Report the malaria status of this cell.
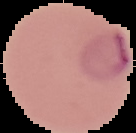
It is parasitized.

The area outside the segmented cell region is set to black. Image is 136×133 pixels. From a thin blood smear.